Locate every uninfected red blood cell.
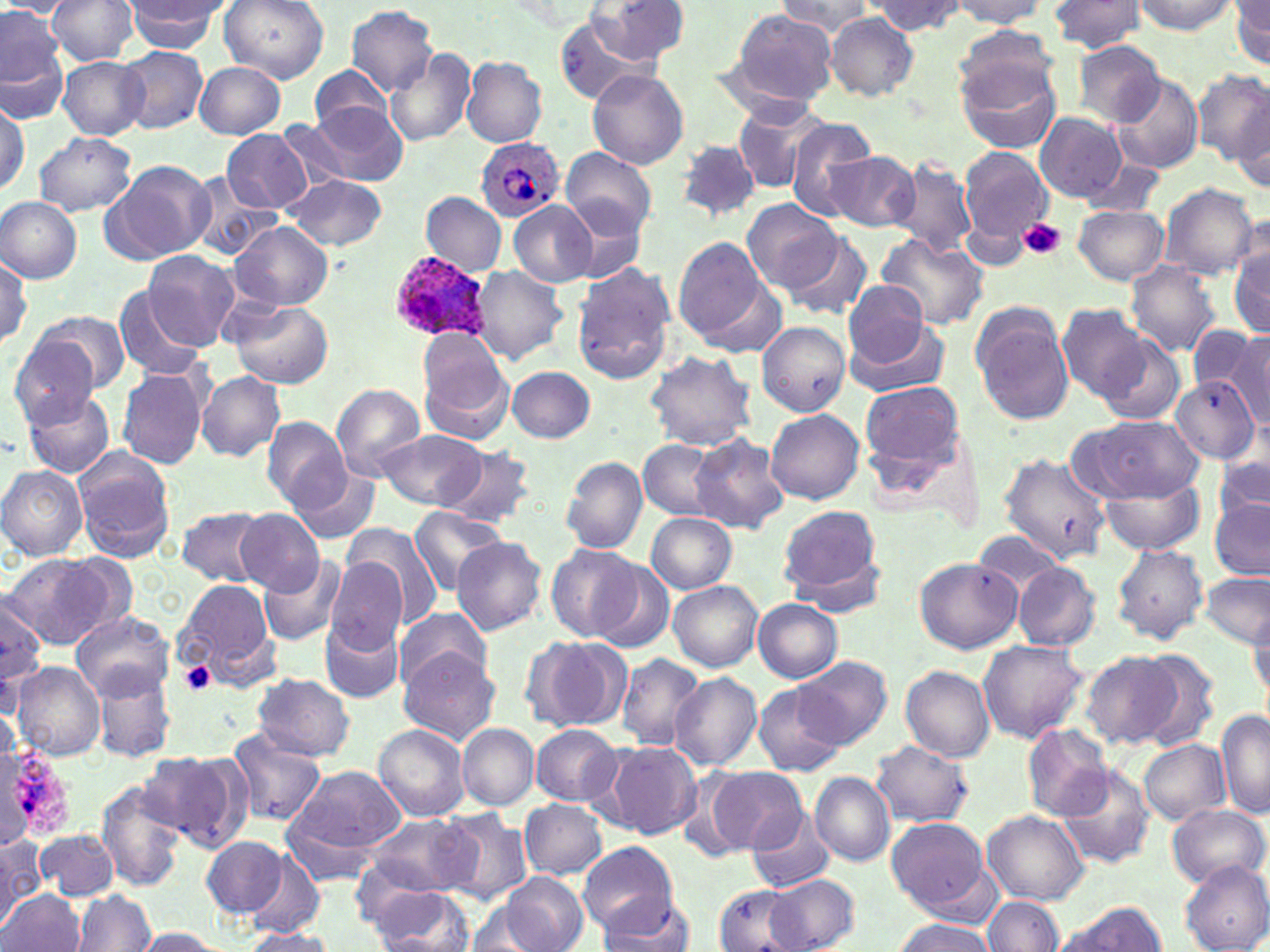

Approximate bounding boxes as named x1/y1/x2/y2 corners in pixels.
Uninfected red blood cells: (x1=46, y1=0, x2=139, y2=67), (x1=219, y1=0, x2=330, y2=82), (x1=949, y1=0, x2=1049, y2=31), (x1=0, y1=1, x2=75, y2=17), (x1=597, y1=1, x2=688, y2=67), (x1=780, y1=1, x2=876, y2=39), (x1=872, y1=1, x2=966, y2=36), (x1=1047, y1=1, x2=1148, y2=53), (x1=1132, y1=1, x2=1238, y2=34), (x1=1231, y1=1, x2=1270, y2=68), (x1=120, y1=2, x2=227, y2=52), (x1=344, y1=5, x2=440, y2=94), (x1=1, y1=8, x2=66, y2=102), (x1=725, y1=9, x2=838, y2=107), (x1=825, y1=12, x2=919, y2=101), (x1=955, y1=23, x2=1056, y2=110), (x1=1072, y1=39, x2=1166, y2=127), (x1=118, y1=46, x2=208, y2=134), (x1=386, y1=49, x2=474, y2=150), (x1=57, y1=55, x2=148, y2=139), (x1=956, y1=56, x2=1062, y2=155), (x1=462, y1=57, x2=547, y2=148), (x1=194, y1=62, x2=286, y2=138), (x1=310, y1=65, x2=399, y2=138), (x1=587, y1=69, x2=689, y2=170), (x1=1194, y1=69, x2=1270, y2=167), (x1=1109, y1=75, x2=1204, y2=176), (x1=308, y1=100, x2=408, y2=186), (x1=0, y1=101, x2=28, y2=194), (x1=730, y1=104, x2=827, y2=193), (x1=1227, y1=105, x2=1269, y2=194), (x1=1034, y1=112, x2=1125, y2=203), (x1=784, y1=115, x2=881, y2=219), (x1=277, y1=119, x2=354, y2=192), (x1=221, y1=127, x2=311, y2=212), (x1=34, y1=132, x2=137, y2=214), (x1=676, y1=140, x2=760, y2=220), (x1=960, y1=147, x2=1054, y2=252), (x1=561, y1=148, x2=656, y2=239), (x1=822, y1=151, x2=920, y2=233), (x1=890, y1=157, x2=977, y2=258), (x1=1076, y1=158, x2=1167, y2=219), (x1=104, y1=159, x2=216, y2=263), (x1=186, y1=174, x2=281, y2=262), (x1=285, y1=175, x2=387, y2=251), (x1=1157, y1=183, x2=1259, y2=280), (x1=422, y1=192, x2=506, y2=273), (x1=0, y1=197, x2=82, y2=282), (x1=743, y1=199, x2=840, y2=293), (x1=508, y1=200, x2=599, y2=287), (x1=1072, y1=204, x2=1170, y2=286), (x1=232, y1=220, x2=333, y2=310), (x1=779, y1=228, x2=874, y2=321), (x1=875, y1=231, x2=988, y2=330), (x1=673, y1=237, x2=769, y2=344), (x1=1229, y1=245, x2=1270, y2=341), (x1=0, y1=249, x2=31, y2=346), (x1=142, y1=249, x2=241, y2=350), (x1=1125, y1=261, x2=1222, y2=357), (x1=571, y1=264, x2=676, y2=386), (x1=470, y1=267, x2=571, y2=366), (x1=697, y1=280, x2=789, y2=358), (x1=842, y1=282, x2=935, y2=372), (x1=112, y1=284, x2=208, y2=381), (x1=224, y1=299, x2=332, y2=388), (x1=970, y1=304, x2=1075, y2=425), (x1=1057, y1=304, x2=1151, y2=402), (x1=841, y1=314, x2=950, y2=400), (x1=25, y1=316, x2=124, y2=401), (x1=757, y1=321, x2=851, y2=417), (x1=1192, y1=325, x2=1267, y2=411), (x1=1227, y1=329, x2=1270, y2=431), (x1=1093, y1=331, x2=1188, y2=425), (x1=9, y1=333, x2=100, y2=431), (x1=417, y1=334, x2=513, y2=440), (x1=645, y1=350, x2=757, y2=452), (x1=507, y1=366, x2=596, y2=443), (x1=117, y1=369, x2=207, y2=468), (x1=197, y1=372, x2=284, y2=461), (x1=1171, y1=377, x2=1259, y2=462), (x1=861, y1=381, x2=965, y2=473), (x1=331, y1=383, x2=424, y2=481), (x1=22, y1=388, x2=117, y2=479), (x1=767, y1=409, x2=863, y2=504), (x1=1074, y1=414, x2=1205, y2=503), (x1=263, y1=418, x2=349, y2=510), (x1=379, y1=430, x2=486, y2=511), (x1=691, y1=435, x2=789, y2=533), (x1=638, y1=438, x2=725, y2=521), (x1=438, y1=444, x2=537, y2=528), (x1=72, y1=446, x2=176, y2=562), (x1=998, y1=447, x2=1123, y2=560), (x1=1213, y1=449, x2=1269, y2=530), (x1=560, y1=455, x2=648, y2=554), (x1=0, y1=464, x2=87, y2=562), (x1=289, y1=467, x2=382, y2=544), (x1=1101, y1=478, x2=1204, y2=553), (x1=1210, y1=497, x2=1269, y2=578), (x1=775, y1=505, x2=887, y2=605), (x1=176, y1=506, x2=270, y2=586), (x1=409, y1=507, x2=510, y2=593), (x1=235, y1=509, x2=322, y2=595), (x1=645, y1=511, x2=736, y2=593), (x1=342, y1=523, x2=442, y2=631), (x1=452, y1=537, x2=547, y2=636), (x1=546, y1=544, x2=642, y2=643), (x1=1112, y1=545, x2=1208, y2=645), (x1=4, y1=554, x2=113, y2=649), (x1=325, y1=557, x2=407, y2=655), (x1=915, y1=557, x2=1021, y2=654), (x1=261, y1=558, x2=347, y2=646), (x1=1013, y1=562, x2=1100, y2=652), (x1=590, y1=563, x2=674, y2=653), (x1=1200, y1=572, x2=1270, y2=648), (x1=173, y1=579, x2=276, y2=683), (x1=669, y1=581, x2=763, y2=673), (x1=0, y1=597, x2=48, y2=688), (x1=754, y1=600, x2=843, y2=682), (x1=393, y1=606, x2=493, y2=690), (x1=1248, y1=606, x2=1270, y2=704), (x1=72, y1=611, x2=173, y2=699), (x1=319, y1=619, x2=404, y2=704), (x1=523, y1=634, x2=632, y2=734), (x1=978, y1=639, x2=1087, y2=743), (x1=399, y1=650, x2=499, y2=746), (x1=1082, y1=650, x2=1184, y2=748), (x1=1135, y1=650, x2=1219, y2=752), (x1=615, y1=653, x2=705, y2=750), (x1=796, y1=657, x2=891, y2=750), (x1=11, y1=660, x2=105, y2=761), (x1=902, y1=664, x2=994, y2=762), (x1=91, y1=665, x2=177, y2=763), (x1=668, y1=672, x2=761, y2=770), (x1=252, y1=673, x2=354, y2=760), (x1=751, y1=681, x2=847, y2=777), (x1=1218, y1=708, x2=1270, y2=820), (x1=1023, y1=723, x2=1113, y2=821), (x1=374, y1=724, x2=469, y2=820), (x1=457, y1=724, x2=538, y2=810), (x1=532, y1=725, x2=621, y2=805), (x1=226, y1=726, x2=326, y2=828), (x1=1139, y1=739, x2=1229, y2=825), (x1=871, y1=741, x2=975, y2=827), (x1=604, y1=743, x2=701, y2=839), (x1=141, y1=751, x2=244, y2=849), (x1=285, y1=763, x2=405, y2=858), (x1=1057, y1=764, x2=1155, y2=869), (x1=702, y1=765, x2=806, y2=857), (x1=810, y1=773, x2=895, y2=865), (x1=96, y1=782, x2=186, y2=891), (x1=520, y1=800, x2=607, y2=878), (x1=1167, y1=804, x2=1268, y2=888), (x1=437, y1=808, x2=534, y2=905), (x1=746, y1=809, x2=832, y2=891), (x1=983, y1=811, x2=1090, y2=905), (x1=360, y1=813, x2=480, y2=900), (x1=886, y1=817, x2=995, y2=920), (x1=37, y1=829, x2=117, y2=900), (x1=0, y1=834, x2=45, y2=920), (x1=202, y1=835, x2=286, y2=918), (x1=579, y1=842, x2=677, y2=937), (x1=244, y1=853, x2=325, y2=935), (x1=1180, y1=861, x2=1270, y2=952), (x1=500, y1=872, x2=587, y2=952), (x1=766, y1=873, x2=859, y2=952), (x1=713, y1=885, x2=801, y2=952), (x1=369, y1=886, x2=465, y2=951), (x1=0, y1=888, x2=84, y2=952), (x1=75, y1=890, x2=156, y2=952), (x1=597, y1=894, x2=696, y2=952), (x1=984, y1=896, x2=1062, y2=950), (x1=465, y1=900, x2=546, y2=949), (x1=1056, y1=900, x2=1167, y2=951), (x1=892, y1=919, x2=997, y2=951), (x1=132, y1=928, x2=229, y2=951), (x1=240, y1=928, x2=338, y2=952).

slide-level diagnosis = Plasmodium ovale
preparation = thin blood film
field of view = one of a larger specimen
Plasmodium ovale-infected red blood cell locations = approximate bounding boxes as named x1/y1/x2/y2 corners in pixels: (x1=476, y1=136, x2=564, y2=221), (x1=390, y1=254, x2=491, y2=342)
stain = May-Grünwald-Giemsa
magnification = 1000x
image size = 1270×952 pixels
platelet locations = approximate bounding boxes as named x1/y1/x2/y2 corners in pixels: (x1=1020, y1=219, x2=1064, y2=260), (x1=180, y1=661, x2=217, y2=694)
modality = optical microscopy